Identify the blood parasite species.
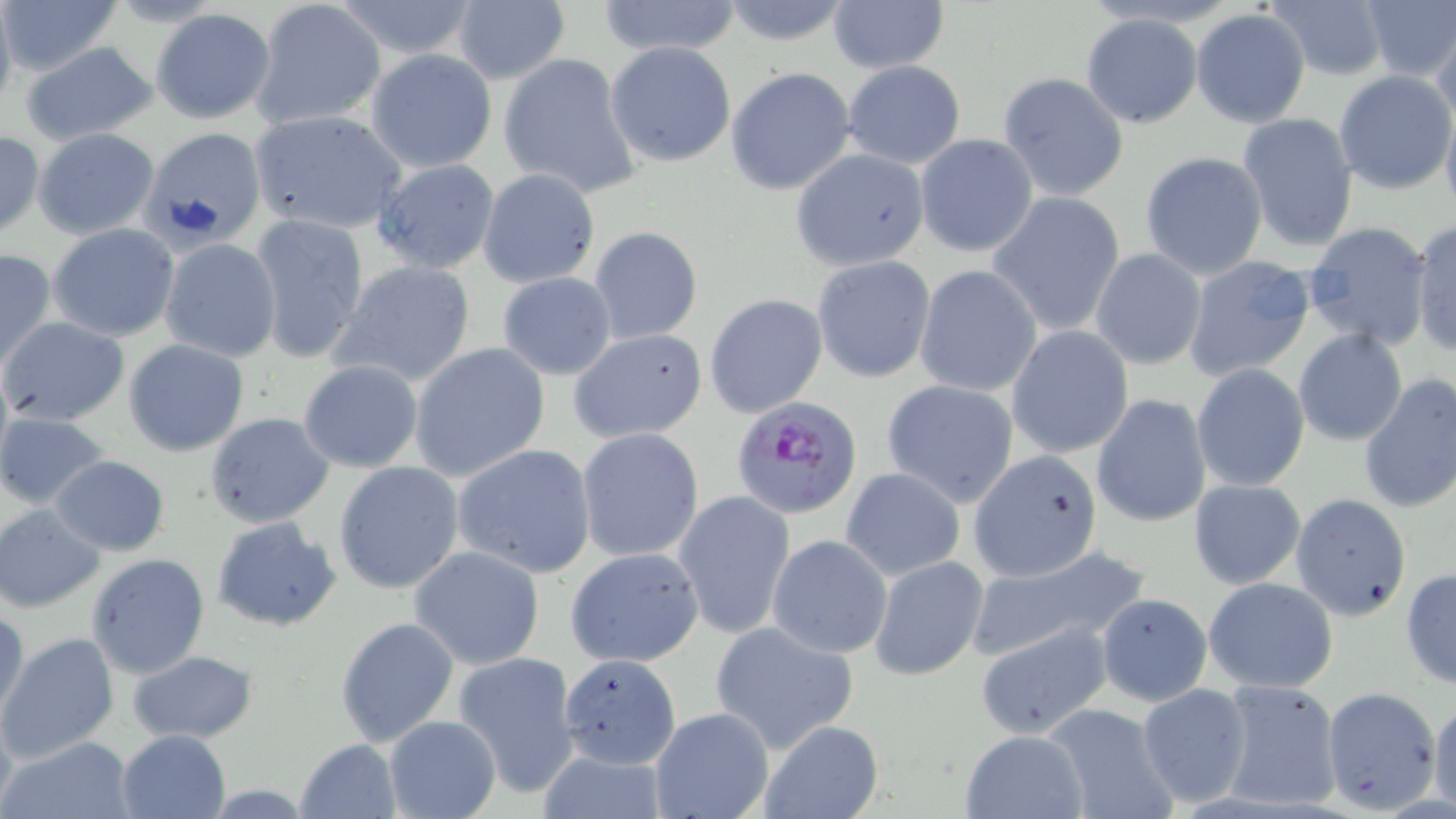
Plasmodium falciparum.

Summary:
  - Coordinate format: approximate bounding boxes as [x1, y1, x2, y2] in pixels
  - Uninfected red blood cell locations: [251, 0, 387, 130], [327, 0, 486, 61], [597, 0, 743, 58], [716, 0, 854, 47], [1264, 0, 1388, 80], [1355, 0, 1455, 84], [1, 1, 121, 78], [827, 1, 948, 74], [451, 3, 571, 86], [1190, 8, 1311, 126], [149, 9, 274, 124], [1079, 12, 1203, 127], [1430, 17, 1456, 138], [21, 42, 159, 147], [605, 42, 737, 169], [365, 48, 499, 173], [498, 53, 640, 198], [841, 61, 967, 169], [725, 67, 855, 195], [1333, 70, 1454, 193], [997, 72, 1129, 200], [1440, 101, 1456, 221], [247, 109, 408, 235], [1237, 111, 1360, 253], [32, 128, 160, 239], [142, 129, 266, 248], [0, 130, 45, 238], [914, 133, 1037, 256], [790, 149, 930, 272], [1139, 150, 1269, 281], [369, 158, 500, 276], [478, 168, 600, 288], [988, 192, 1125, 335], [249, 213, 370, 363], [1409, 219, 1456, 358], [1302, 222, 1434, 352], [49, 223, 181, 342], [588, 226, 705, 346], [159, 238, 282, 360], [0, 248, 57, 373], [1090, 248, 1208, 371], [1180, 253, 1317, 383], [811, 255, 936, 383], [330, 260, 477, 389], [914, 263, 1043, 398], [497, 271, 617, 380], [704, 292, 828, 418], [2, 316, 130, 426], [1006, 326, 1134, 459], [570, 327, 707, 443], [1293, 329, 1408, 447], [123, 338, 250, 457], [408, 343, 550, 481], [298, 359, 424, 473], [1192, 365, 1309, 492], [1356, 373, 1456, 515], [881, 378, 1019, 506], [1091, 394, 1212, 529], [1, 412, 110, 509], [205, 413, 336, 528], [577, 428, 704, 562], [453, 443, 598, 579], [966, 450, 1104, 581], [50, 455, 169, 556], [333, 461, 465, 595], [841, 467, 966, 579], [1187, 479, 1307, 590], [674, 490, 795, 639], [1290, 493, 1412, 620], [1, 503, 105, 612], [212, 516, 342, 632], [767, 534, 894, 658], [972, 545, 1152, 659], [410, 547, 546, 670], [565, 547, 705, 667], [86, 553, 211, 680], [869, 556, 989, 682], [1401, 566, 1456, 692], [1203, 576, 1339, 692], [1094, 593, 1212, 706], [0, 604, 28, 724], [334, 617, 459, 748], [710, 621, 859, 754], [976, 623, 1113, 741], [0, 632, 120, 762], [126, 650, 260, 743], [452, 651, 582, 797], [1216, 679, 1344, 811], [1136, 683, 1252, 807], [1321, 686, 1443, 814], [1430, 698, 1456, 811], [1043, 702, 1179, 818], [649, 707, 774, 819], [384, 715, 502, 819], [760, 722, 883, 816], [116, 729, 231, 819], [957, 729, 1090, 819], [4, 735, 137, 818], [295, 738, 401, 818], [534, 747, 670, 819]
  - Plasmodium falciparum-infected red blood cell locations: [732, 395, 863, 519]
  - Field of view: single
  - Preparation: thin blood smear
  - Image size: 1456×819 pixels
  - Magnification: 1000x
  - Modality: optical microscopy
  - Stain: May-Grünwald-Giemsa